Point out each Plasmodium parasite.
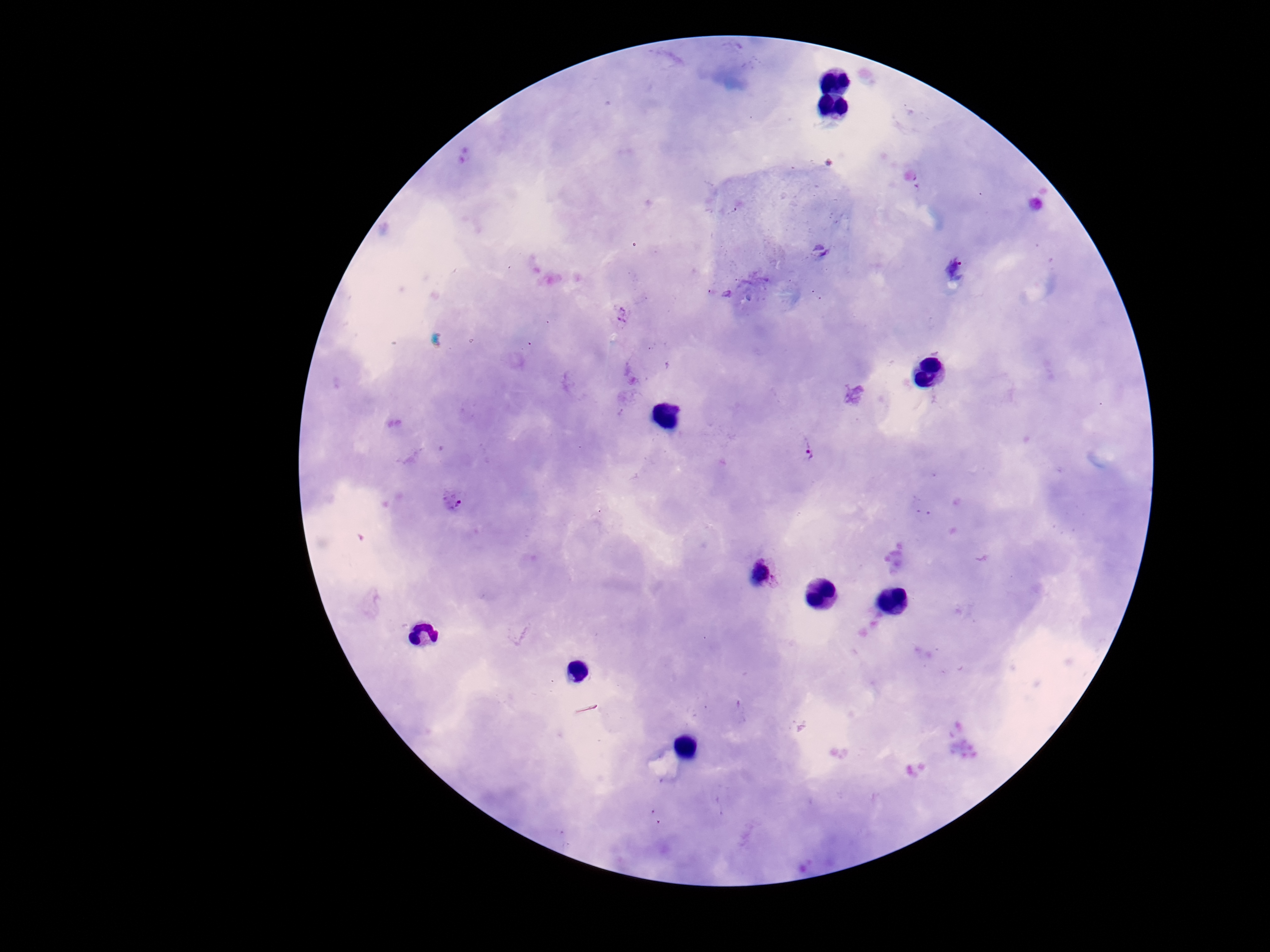

Approximate centers as (x, y) in pixels.
Plasmodium parasites: (807, 450), (453, 502), (763, 574).

stain = Giemsa
image size = 1270×952 pixels
patient malaria status = infected
magnification = 100x
field of view = single
capture = smartphone camera through the microscope eyepiece
preparation = thick blood film